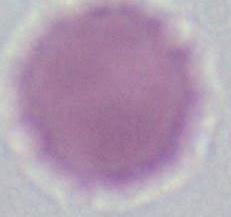

Captured at 1000x magnification. Micrograph. An erythrocyte is shown.